Describe the morphology of the red blood cells.
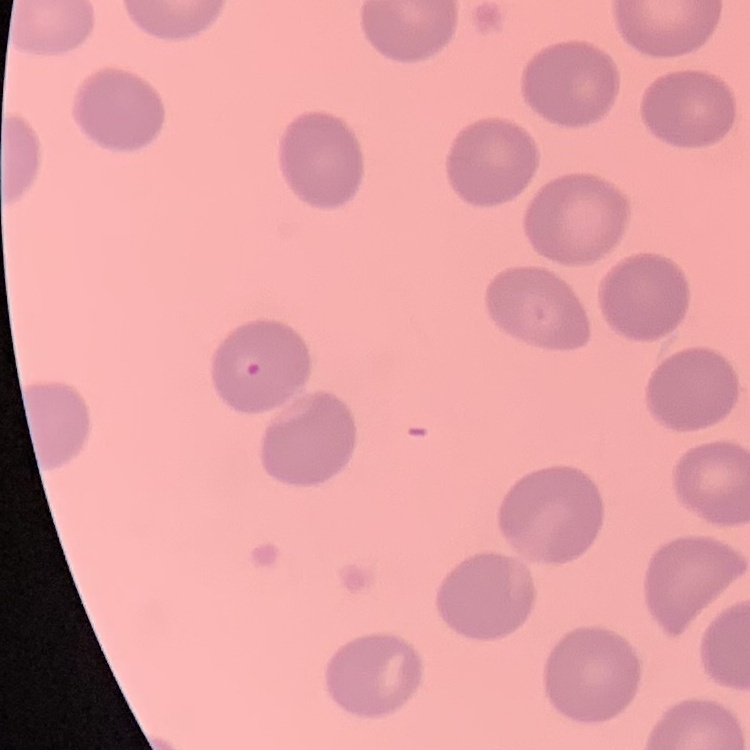

They show no rouleaux formation.

Summary:
  - Image type: square crop of a larger photomicrograph
  - Preparation: thin blood film
  - Stain: Field's or Giemsa